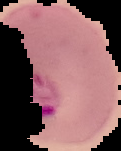

Summary:
  - Image size: 121×151 pixels
  - Result: malaria parasites identified
  - Preparation: thin blood smear
  - Image type: segmented cell region on a black background